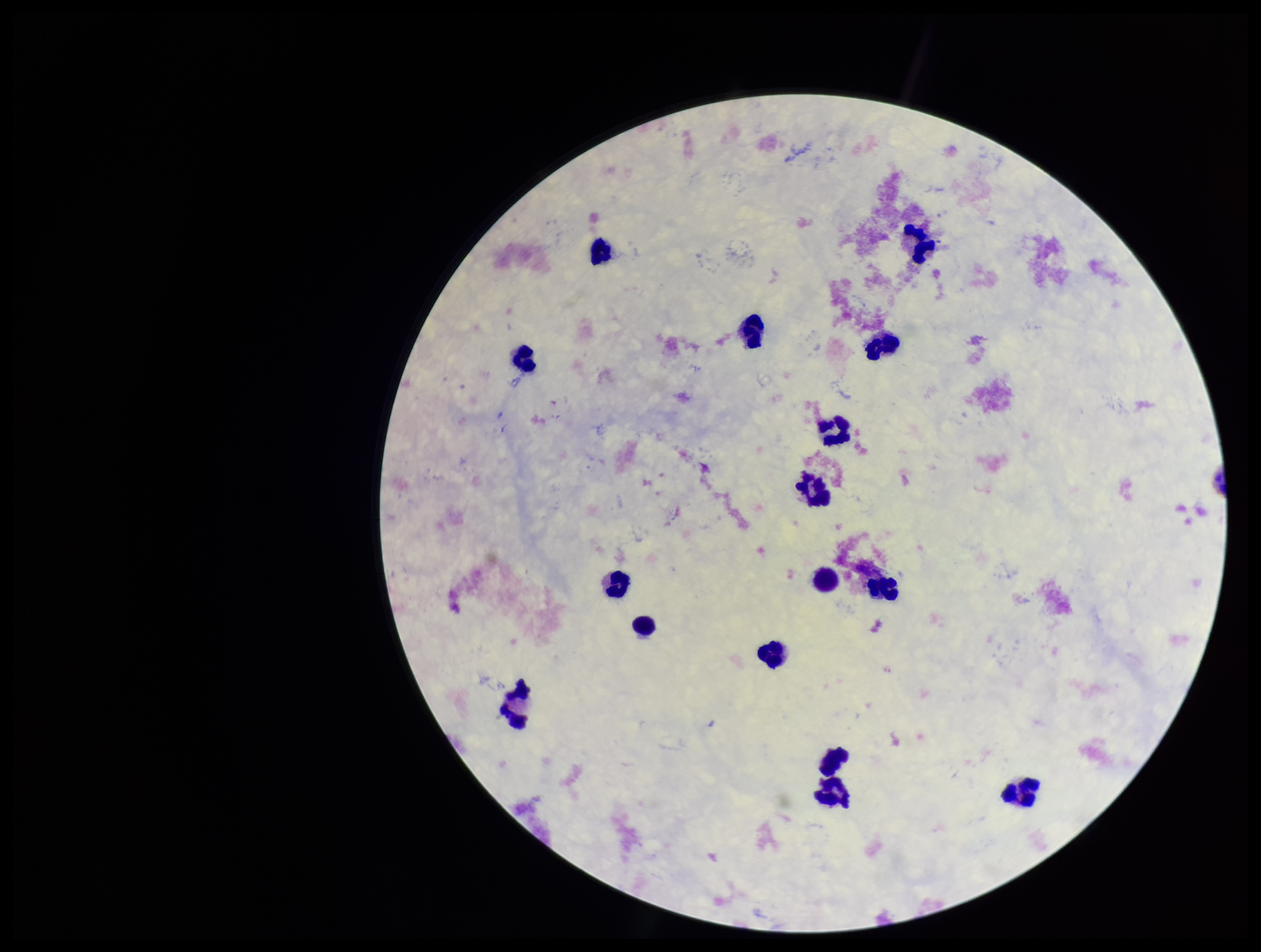

Summary:
  - Patient malaria status: negative
  - Stain: Giemsa
  - Preparation: thick smear
  - Capture: smartphone photograph through the microscope eyepiece
  - Leukocyte count: 16
  - Parasite count: 0
  - Field of view: single
  - Plasmodium parasites: none detected
  - Image size: 1261×952 pixels